Assess for Plasmodium parasites.
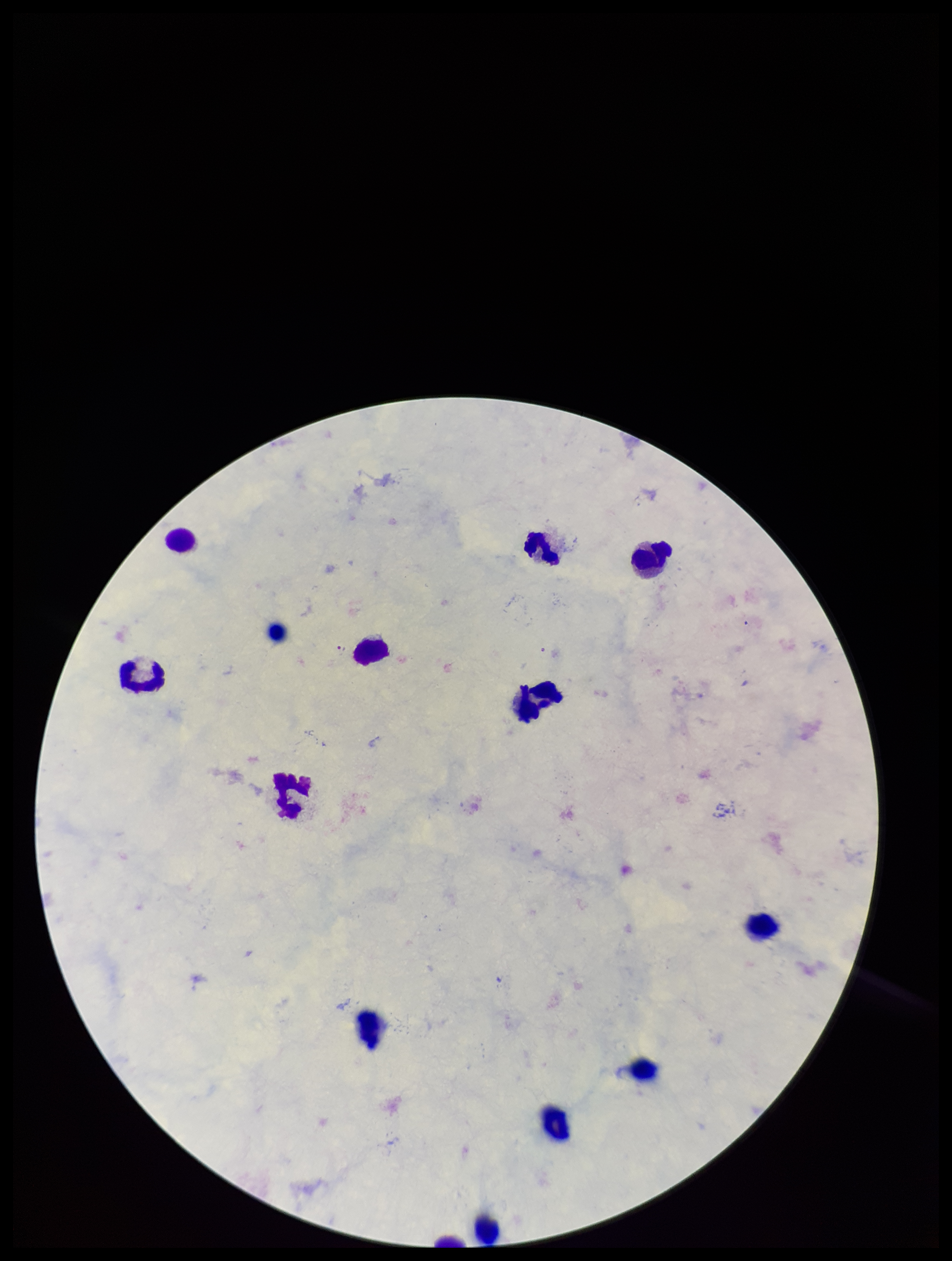
Seen.

{
  "parasite_count": 1,
  "species_reported_for_this_patient": "Plasmodium falciparum",
  "leukocyte_count": 13,
  "field_of_view": "one from this slide",
  "image_size": "952×1261 pixels",
  "capture": "smartphone photograph through the microscope eyepiece",
  "preparation": "thick blood smear",
  "patient_malaria_status": "positive",
  "stain": "Giemsa"
}